Locate every Plasmodium parasite.
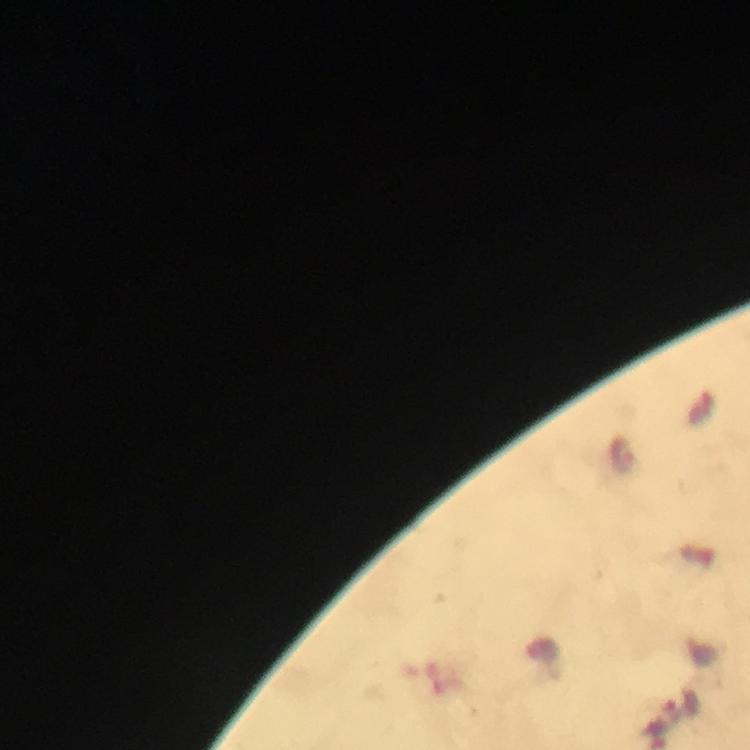

Approximate centers as {x, y} in pixels.
Plasmodium parasites: {623, 454}, {683, 704}.

Summary:
  - Context: from a diagnostic examination for malaria
  - Cropped from: a single field of view
  - Immersion oil: applied
  - Capture: smartphone photograph through a microscope
  - Stain: Giemsa
  - Preparation: thick smear
  - Magnification: 100x
  - Image size: 750×750 pixels